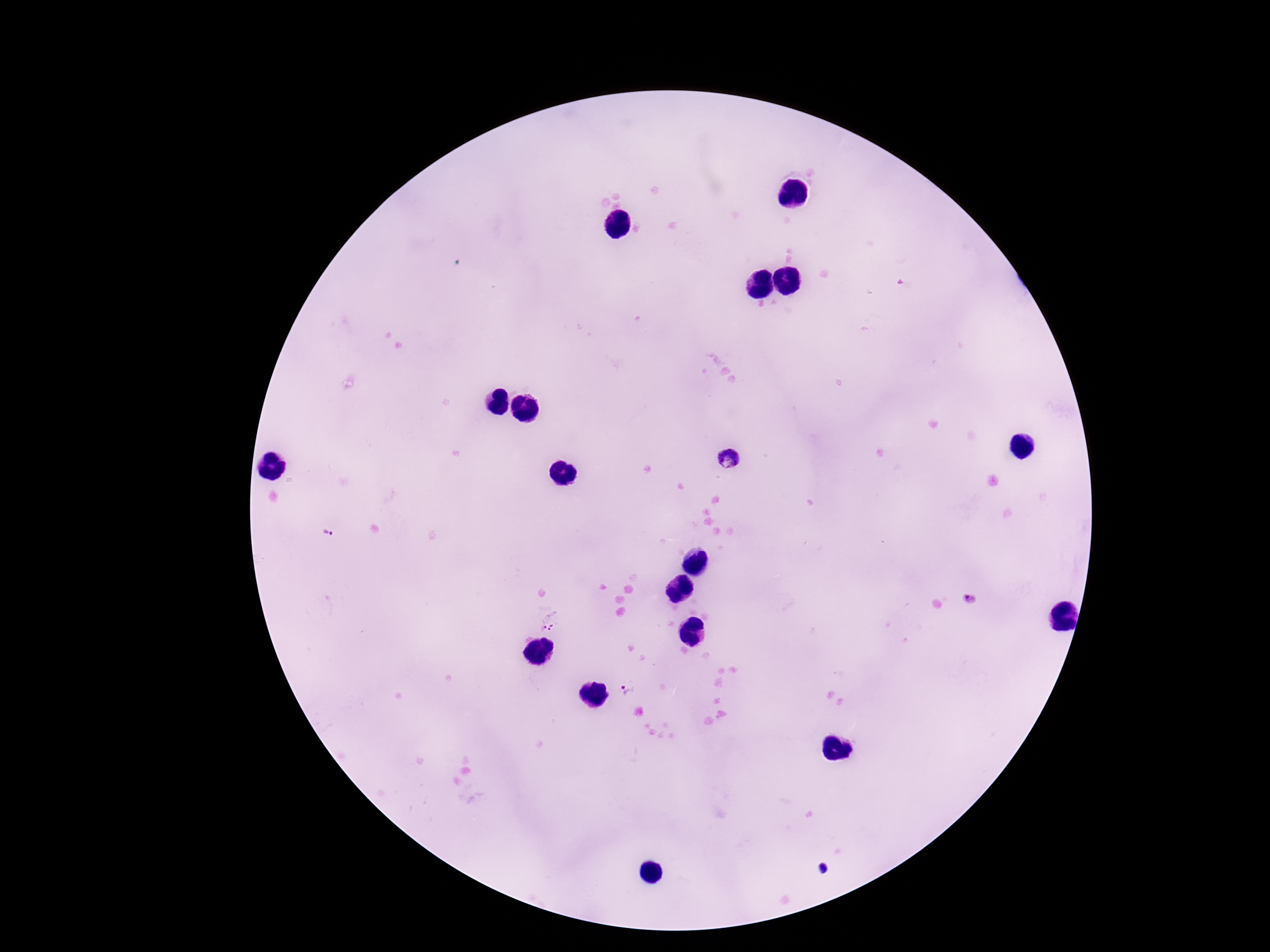
Approximate object centers, in pixels from the top-left corner.
Summary:
  - Plasmodium parasite locations: (x=729, y=459), (x=328, y=535), (x=968, y=598), (x=549, y=620), (x=628, y=690)
  - Stain: Giemsa
  - Patient malaria status: positive
  - Magnification: 100x
  - Field of view: one from this slide
  - Capture: smartphone camera through the microscope eyepiece
  - Preparation: thick blood smear
  - Image size: 1270×952 pixels